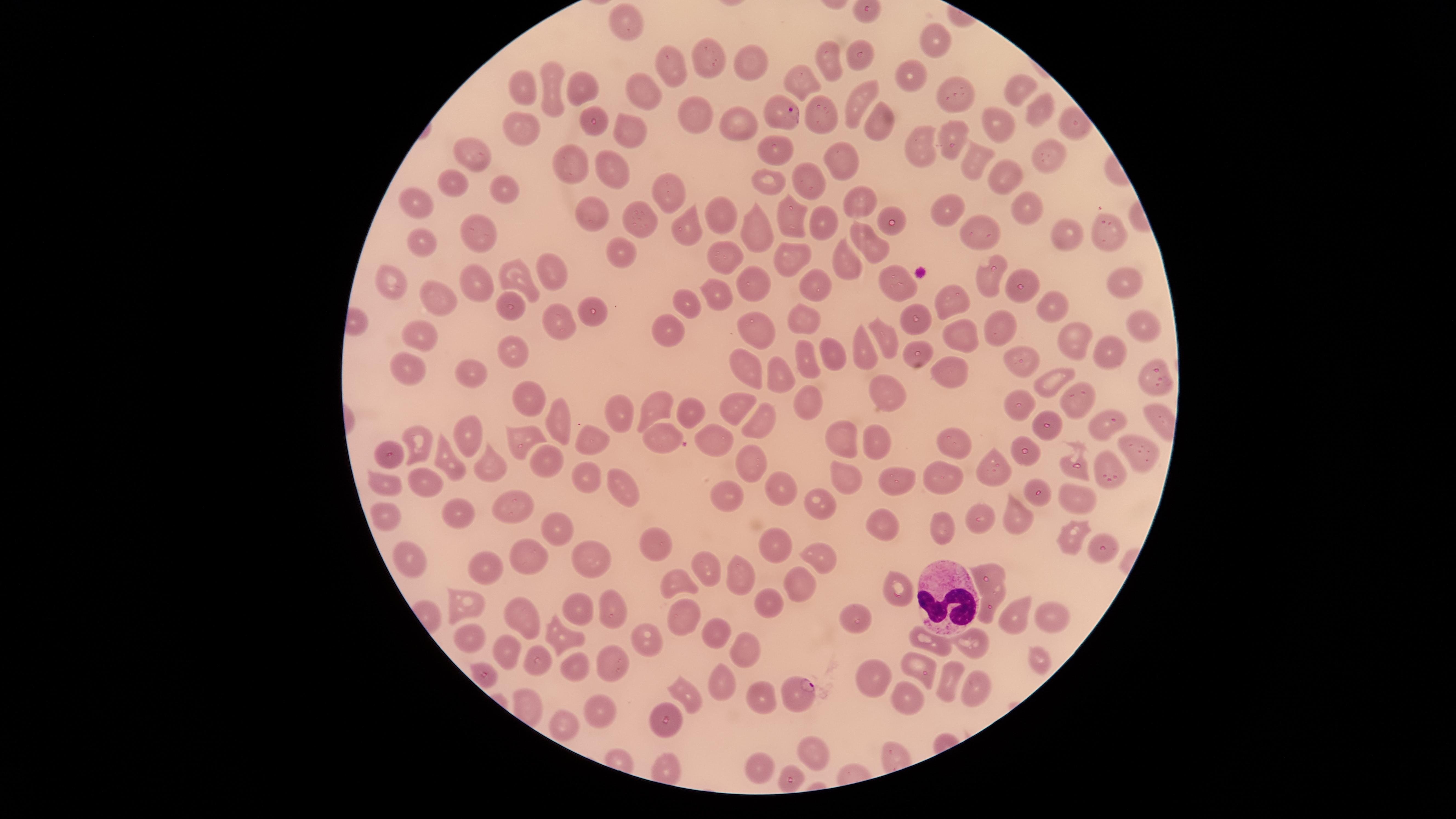
{
  "presence": "malaria parasites detected",
  "stain": "Giemsa",
  "field_of_view": "single",
  "species": "Plasmodium falciparum",
  "parasitized_red_blood_cells": "approximate marker points as (x, y) in pixels: (781, 110), (798, 692)",
  "capture": "smartphone photograph through the microscope eyepiece",
  "white_blood_cells": "approximate marker points as (x, y) in pixels: (940, 586)",
  "uninfected_red_blood_cells": "approximate marker points as (x, y) in pixels: (623, 19), (941, 42), (858, 53), (831, 60), (709, 61), (751, 65), (668, 68), (912, 74), (804, 80), (524, 88), (581, 89), (646, 90), (549, 92), (1019, 93), (956, 95), (859, 99), (1038, 110), (827, 115), (699, 116), (592, 119), (737, 123), (879, 123), (1070, 124), (519, 126), (996, 127), (624, 130), (954, 132), (920, 146), (472, 150), (774, 151), (840, 156), (1048, 156), (967, 159), (612, 168), (581, 169), (996, 174), (763, 179), (803, 179), (454, 181), (509, 190), (670, 196), (856, 199), (418, 201), (891, 209), (946, 209), (717, 210), (791, 212), (1028, 212), (596, 214), (643, 217), (823, 219), (689, 227), (1105, 228), (980, 231), (478, 232), (1065, 234), (758, 235), (421, 237), (871, 241), (720, 252), (620, 254), (792, 255), (843, 260), (548, 268), (983, 277), (814, 278), (524, 279), (483, 280), (887, 281), (1119, 281), (386, 284), (758, 284), (1022, 284), (713, 295), (951, 298), (437, 300), (689, 301), (509, 302), (594, 307), (1050, 307), (915, 310), (552, 312), (804, 319), (1142, 322), (1002, 327), (420, 330), (670, 330), (754, 330), (884, 333), (967, 333), (1066, 341), (861, 347), (514, 348), (806, 354), (835, 354), (1107, 354), (915, 363), (411, 364), (1025, 364), (739, 368), (949, 369), (478, 372), (783, 372), (1049, 378), (1151, 379), (892, 393), (532, 395), (1075, 398), (1015, 400), (808, 402), (733, 407), (662, 408), (619, 410), (687, 410), (763, 414), (564, 421), (1109, 421), (464, 429), (1054, 429), (663, 434), (720, 434), (844, 434), (531, 440), (870, 441), (1022, 441), (422, 442), (590, 442), (958, 442), (1138, 447), (392, 450), (442, 452), (750, 453), (544, 460), (493, 462), (996, 466), (1109, 468), (1080, 470), (845, 474), (584, 476), (783, 478), (949, 478), (425, 482), (898, 482), (390, 485), (624, 488), (725, 494), (1072, 495), (815, 501), (517, 504), (458, 508), (1013, 509), (982, 514), (384, 517), (881, 519), (558, 525), (942, 531), (1071, 534), (656, 538), (776, 547), (1097, 547), (530, 555), (595, 558), (416, 559), (815, 559), (487, 563), (715, 566), (989, 572), (736, 574), (678, 577), (797, 587), (892, 590), (604, 599), (464, 602), (576, 602), (770, 603), (991, 607), (682, 612), (524, 614), (1048, 614), (1010, 615), (862, 619), (715, 632), (470, 638), (569, 638), (649, 638), (975, 639), (924, 640), (747, 647), (507, 651), (610, 656), (541, 657), (1037, 657), (577, 664), (919, 666), (482, 671), (872, 677), (981, 684), (714, 685), (947, 685), (689, 690), (761, 696), (903, 704), (601, 705), (662, 713), (560, 728), (813, 748), (760, 768)",
  "image_size": "1456×819 pixels",
  "visible_region": "circular",
  "preparation": "thin blood film"
}